Classify this cell by malaria status.
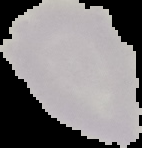

It is uninfected.

Cell region segmented out of the field of view; the surrounding area is masked to black. From a thin blood smear. Image is 142×148 pixels.